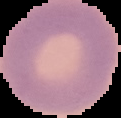
From a thin blood smear. Result: no Plasmodium parasites seen. Segmented cell region on a black background. Image is 121×118 pixels.